State the blood parasite species.
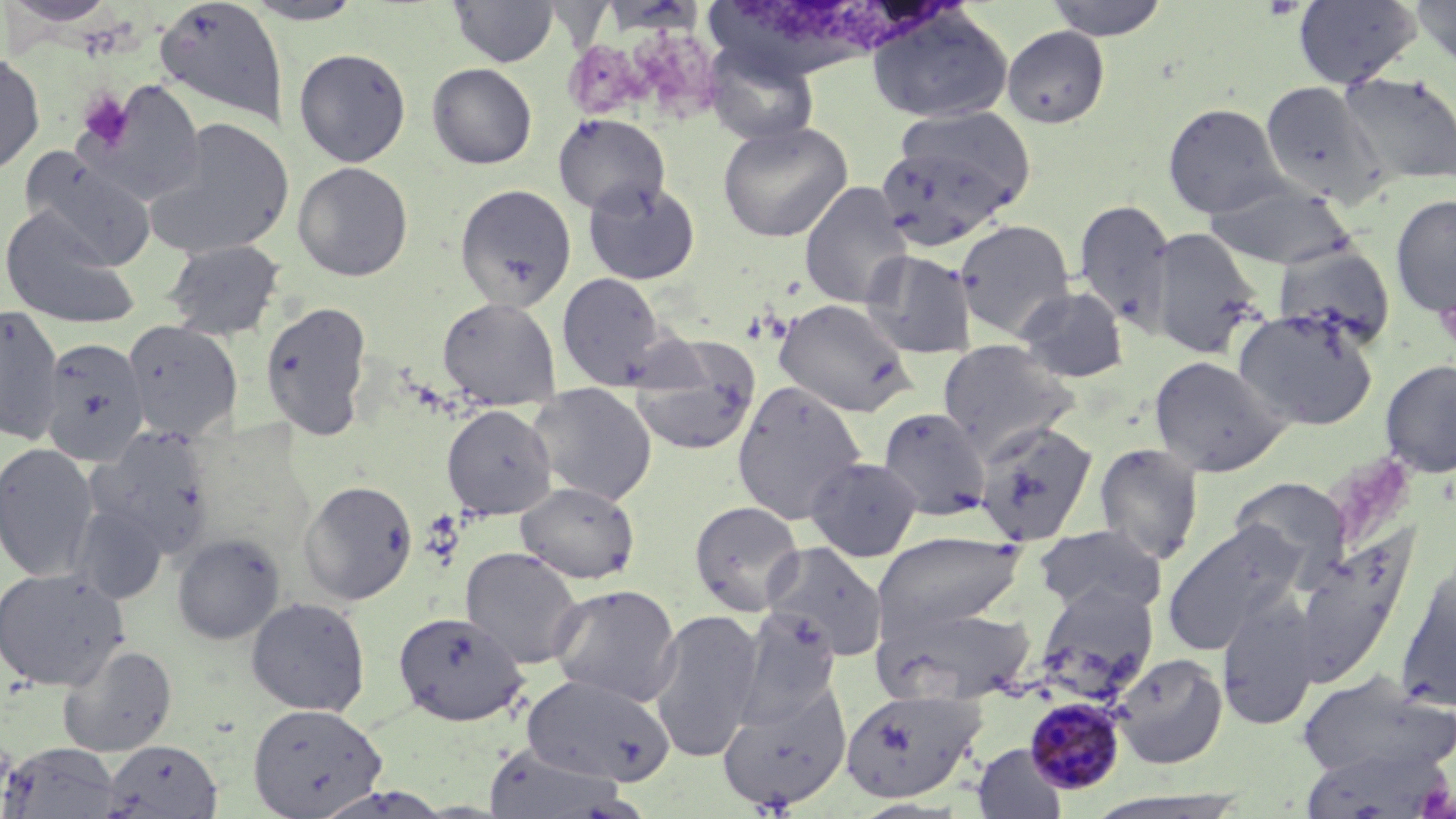

Plasmodium malariae.

platelet locations = approximate bounding boxes as (x1, y1, x2, y2) in pixels: (1261, 0, 1304, 20), (76, 88, 135, 151)
uninfected red blood cell locations = approximate bounding boxes as (x1, y1, x2, y2) in pixels: (154, 0, 288, 128), (449, 0, 559, 67), (1043, 0, 1170, 40), (1293, 0, 1422, 88), (1413, 0, 1456, 72), (2, 1, 124, 28), (241, 1, 368, 25), (867, 7, 1013, 124), (1002, 25, 1110, 129), (704, 41, 820, 146), (293, 47, 411, 167), (0, 51, 45, 177), (427, 63, 537, 169), (1338, 72, 1456, 187), (75, 81, 206, 206), (1259, 81, 1388, 207), (1162, 102, 1287, 218), (897, 106, 1037, 210), (553, 113, 670, 217), (145, 118, 293, 260), (717, 119, 853, 242), (874, 142, 1013, 252), (20, 149, 157, 271), (292, 161, 413, 282), (582, 178, 701, 286), (1205, 180, 1356, 270), (799, 181, 913, 309), (454, 183, 577, 311), (1390, 193, 1456, 318), (1074, 199, 1176, 328), (0, 205, 141, 330), (954, 218, 1076, 340), (1148, 227, 1265, 359), (162, 239, 286, 341), (1273, 244, 1396, 346), (861, 249, 977, 359), (556, 272, 671, 390), (1016, 285, 1130, 383), (437, 296, 561, 409), (773, 298, 917, 418), (259, 299, 373, 440), (0, 302, 65, 445), (1232, 308, 1378, 430), (122, 319, 242, 443), (627, 336, 761, 456), (39, 338, 150, 465), (936, 339, 1079, 455), (1148, 355, 1291, 478), (1379, 358, 1456, 478), (732, 380, 867, 526), (527, 383, 657, 506), (441, 404, 557, 519), (877, 407, 991, 520), (974, 422, 1099, 546), (87, 427, 217, 558), (1093, 441, 1205, 564), (0, 442, 99, 583), (805, 455, 923, 562), (1227, 477, 1353, 584), (299, 479, 418, 605), (515, 481, 640, 584), (689, 500, 806, 616), (69, 504, 168, 604), (1162, 522, 1301, 656), (1032, 523, 1167, 617), (872, 532, 1028, 636), (171, 533, 285, 645), (1292, 533, 1416, 682), (761, 542, 889, 660), (460, 547, 584, 669), (1394, 556, 1456, 710), (0, 567, 129, 691), (548, 583, 682, 707), (1035, 583, 1160, 695), (1217, 593, 1319, 731), (246, 596, 371, 716), (735, 605, 842, 723), (877, 605, 1037, 705), (647, 609, 762, 762), (393, 610, 528, 725), (59, 644, 177, 757), (1112, 653, 1228, 769), (1295, 669, 1456, 782), (520, 673, 674, 786), (718, 682, 852, 811), (841, 688, 986, 804), (248, 703, 387, 817), (103, 739, 223, 818), (1, 742, 121, 818), (481, 743, 633, 818), (973, 743, 1068, 819), (1299, 743, 1453, 819), (309, 785, 456, 818)
image size = 1456×819 pixels
Plasmodium malariae-infected red blood cell locations = approximate bounding boxes as (x1, y1, x2, y2) in pixels: (1025, 696, 1127, 795)
field of view = single
stain = May-Grünwald-Giemsa
magnification = 1000x
modality = light microscopy
preparation = thin blood film